Assess this cell for malaria.
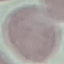

It is uninfected.

Thin smear of blood. Acquired by smartphone through the microscope eyepiece. Giemsa stain. Cell patch, automatically extracted from a larger field of view and resized to 64 × 64 pixels.